Assess for Plasmodium parasites.
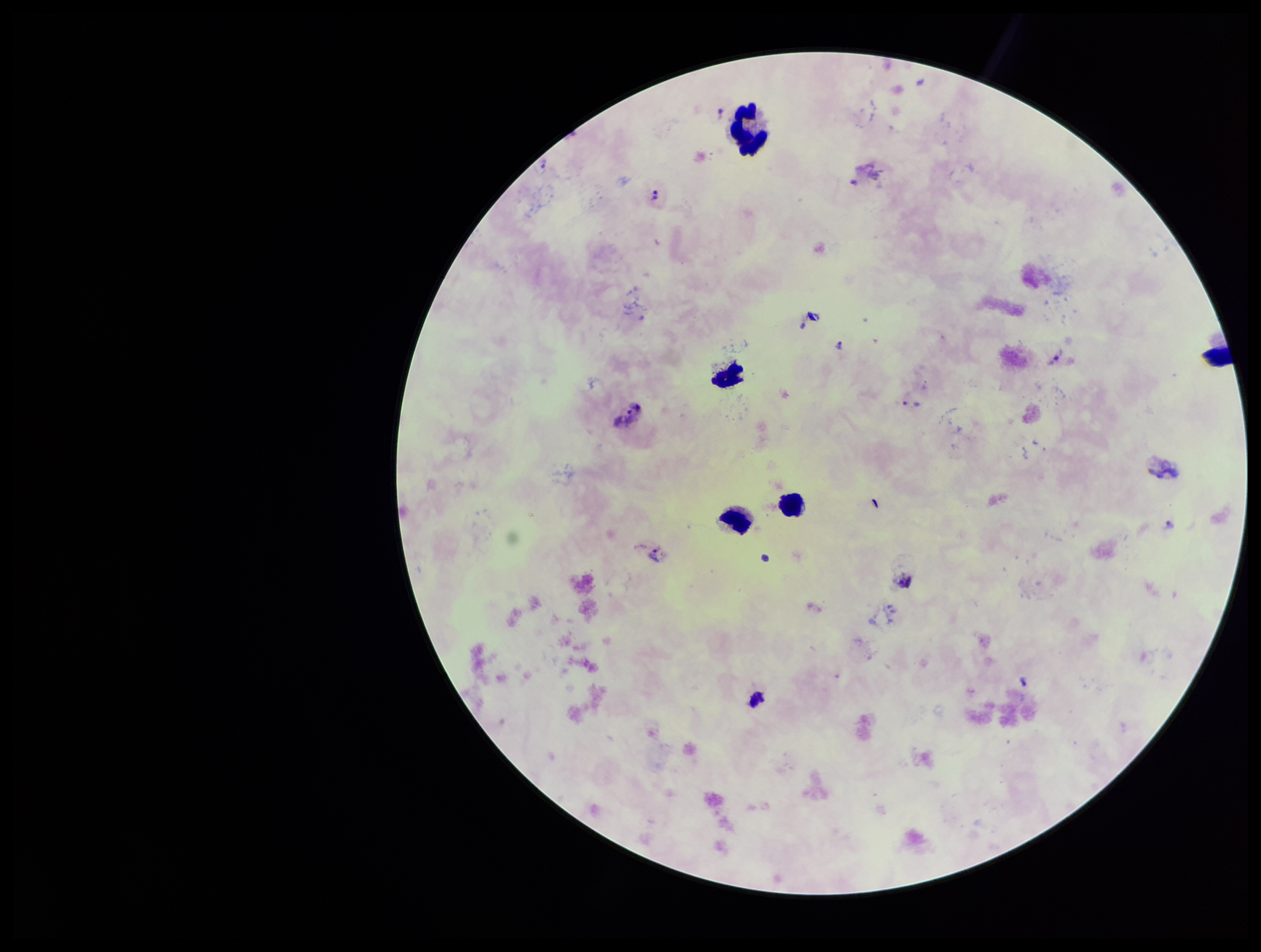
Identified.

Summary:
  - Species reported for this patient: Plasmodium vivax
  - Image size: 1261×952 pixels
  - Stain: Giemsa
  - Preparation: thick
  - Leukocyte count: 5
  - Field of view: one from this slide
  - Capture: smartphone photograph through the microscope eyepiece
  - Patient malaria status: infected
  - Parasite count: 6